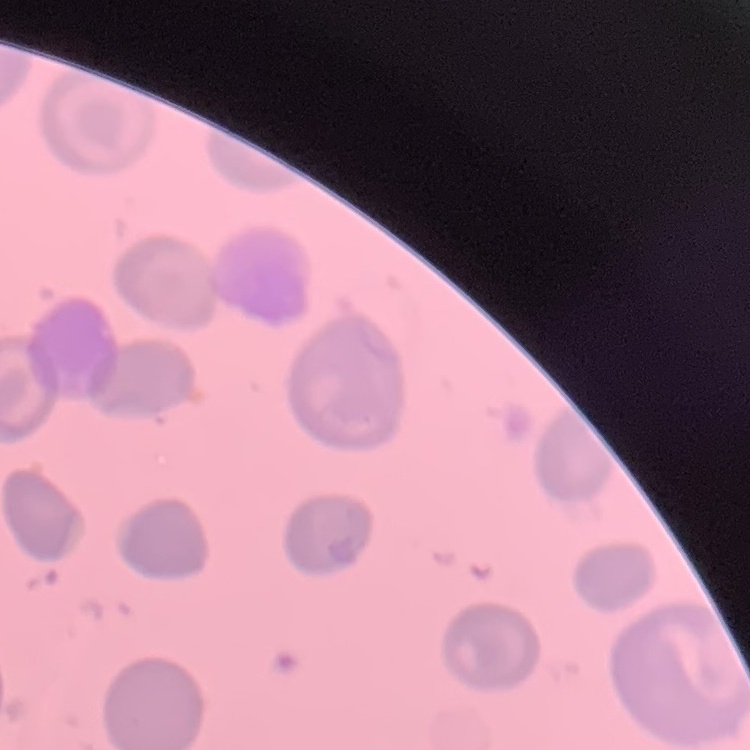

Summary:
  - Erythrocyte morphology: no rouleaux formation
  - Stain: Field's or Giemsa
  - Preparation: thin peripheral smear
  - Image type: one tile cut from a larger photomicrograph